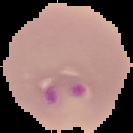
Summary:
  - Image size: 133×133 pixels
  - Image type: segmented cell region with the area outside set to black
  - Malaria status: parasitized
  - Preparation: thin blood smear